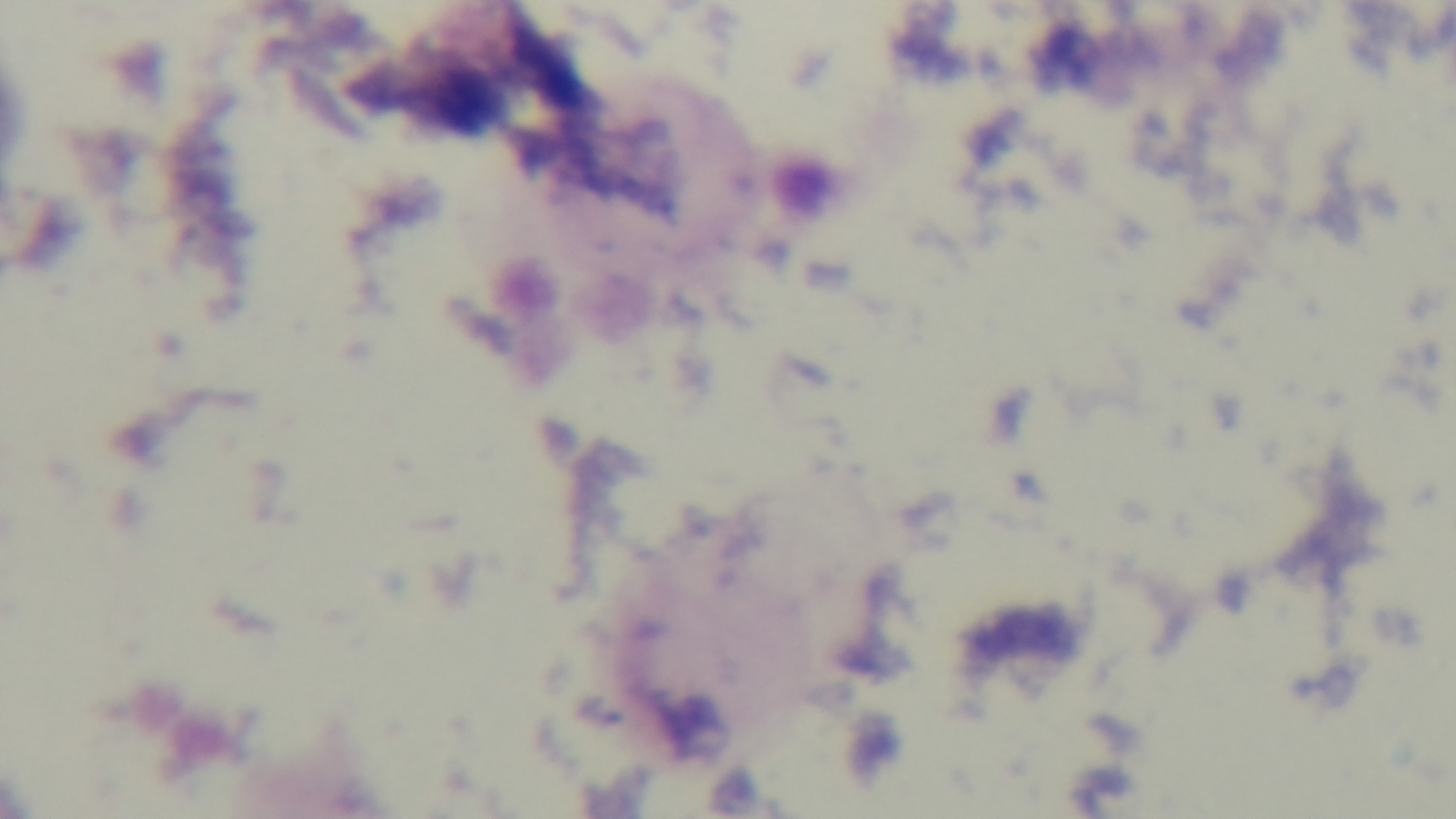

Summary:
  - Stain: Giemsa
  - Preparation: thick blood film
  - Malaria status: uninfected
  - Capture: mounted 4K digital camera
  - Objective: 100x oil immersion
  - Modality: light microscopy
  - Field of view: one from the slide